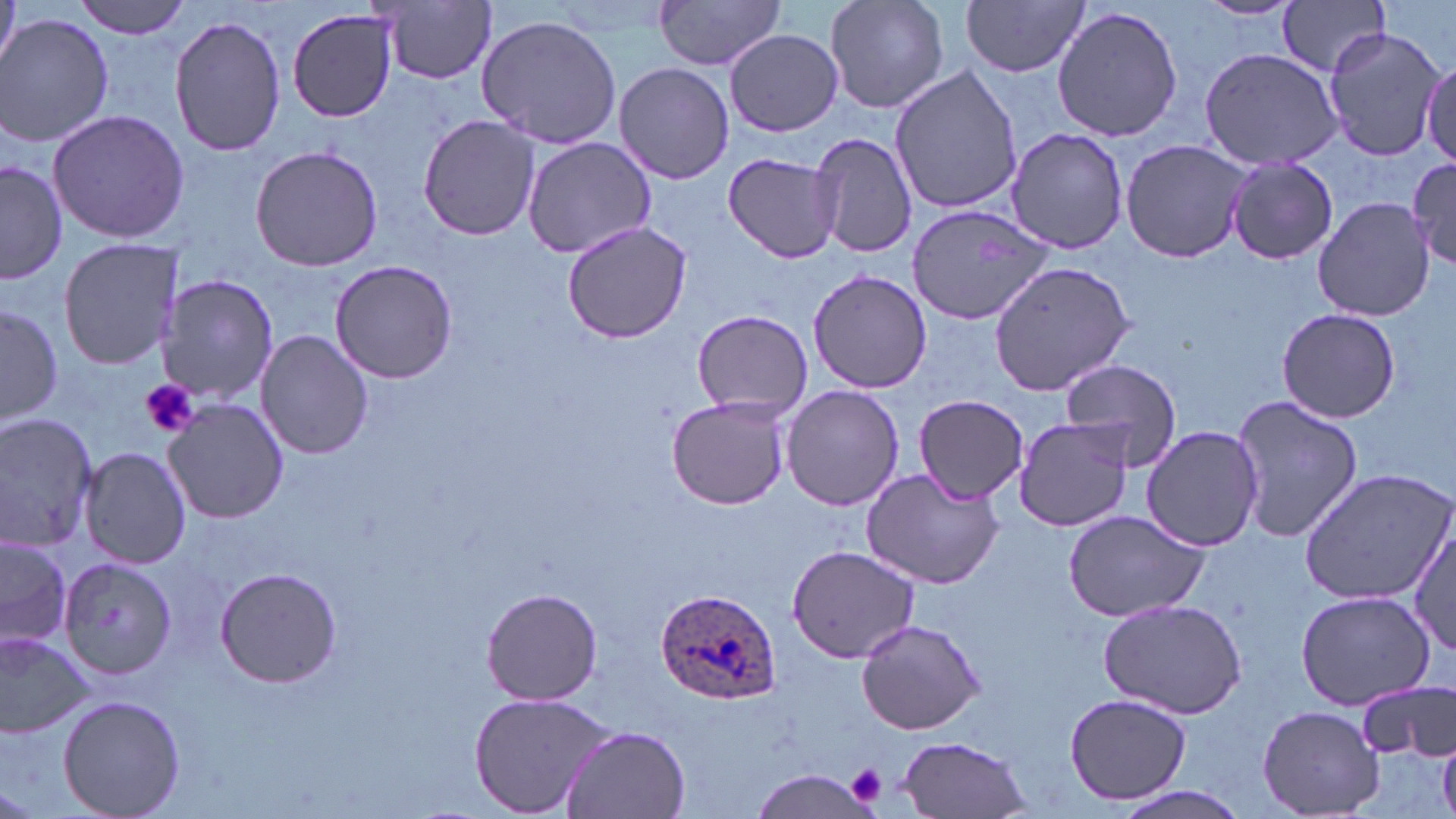
slide-level diagnosis = Plasmodium ovale
image size = 1456×819 pixels
platelet locations = approximate bounding boxes as (x1, y1, x2, y2) in pixels: (140, 378, 199, 438), (848, 764, 886, 802)
uninfected red blood cell locations = approximate bounding boxes as (x1, y1, x2, y2) in pixels: (70, 0, 194, 39), (654, 0, 787, 71), (823, 0, 949, 115), (962, 0, 1090, 77), (1196, 0, 1302, 21), (1278, 0, 1391, 77), (0, 1, 20, 73), (378, 1, 500, 85), (1052, 5, 1184, 142), (286, 7, 400, 123), (169, 14, 287, 160), (1, 15, 115, 147), (476, 15, 624, 150), (1321, 24, 1447, 163), (726, 30, 843, 136), (1196, 46, 1344, 172), (1422, 55, 1456, 165), (613, 62, 734, 184), (888, 65, 1024, 216), (46, 109, 190, 244), (418, 115, 541, 242), (1006, 127, 1129, 254), (809, 130, 917, 259), (522, 136, 661, 261), (1119, 138, 1255, 266), (249, 145, 383, 272), (722, 150, 844, 264), (1408, 155, 1456, 270), (1226, 159, 1338, 265), (1, 160, 69, 283), (1312, 196, 1434, 320), (907, 204, 1056, 325), (562, 220, 693, 343), (58, 237, 183, 371), (329, 258, 457, 385), (988, 259, 1137, 394), (807, 268, 932, 393), (157, 275, 277, 405), (0, 302, 63, 426), (1275, 306, 1401, 424), (691, 309, 813, 419), (256, 328, 374, 461), (1059, 361, 1183, 469), (781, 384, 904, 511), (1229, 393, 1363, 545), (913, 394, 1028, 501), (667, 395, 790, 511), (163, 399, 291, 523), (0, 412, 100, 551), (1012, 415, 1136, 532), (1140, 425, 1265, 552), (78, 446, 190, 570), (1297, 467, 1456, 605), (862, 469, 1004, 590), (1060, 505, 1212, 624), (1408, 524, 1456, 656), (0, 534, 73, 651), (786, 543, 921, 664), (60, 558, 177, 679), (213, 568, 341, 688), (483, 587, 603, 705), (1297, 588, 1436, 710), (1099, 597, 1248, 718), (853, 616, 986, 736), (0, 631, 93, 738), (1357, 679, 1456, 762), (466, 690, 620, 818), (1065, 693, 1191, 807), (57, 695, 186, 819), (1258, 704, 1387, 817), (561, 724, 693, 818), (894, 735, 1034, 818), (752, 767, 879, 817), (1102, 784, 1254, 819)
stain = May-Grünwald-Giemsa
magnification = 1000x
preparation = thin blood film
Plasmodium ovale-infected red blood cell locations = approximate bounding boxes as (x1, y1, x2, y2) in pixels: (655, 589, 781, 707)
modality = optical microscopy
field of view = one of a larger specimen